Classify this cell by malaria status.
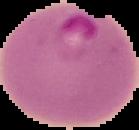

It is parasitized.

Segmented cell region on a black background. Image is 139×130 pixels. From a thin blood film.